Locate every leukocyte (white blood cell).
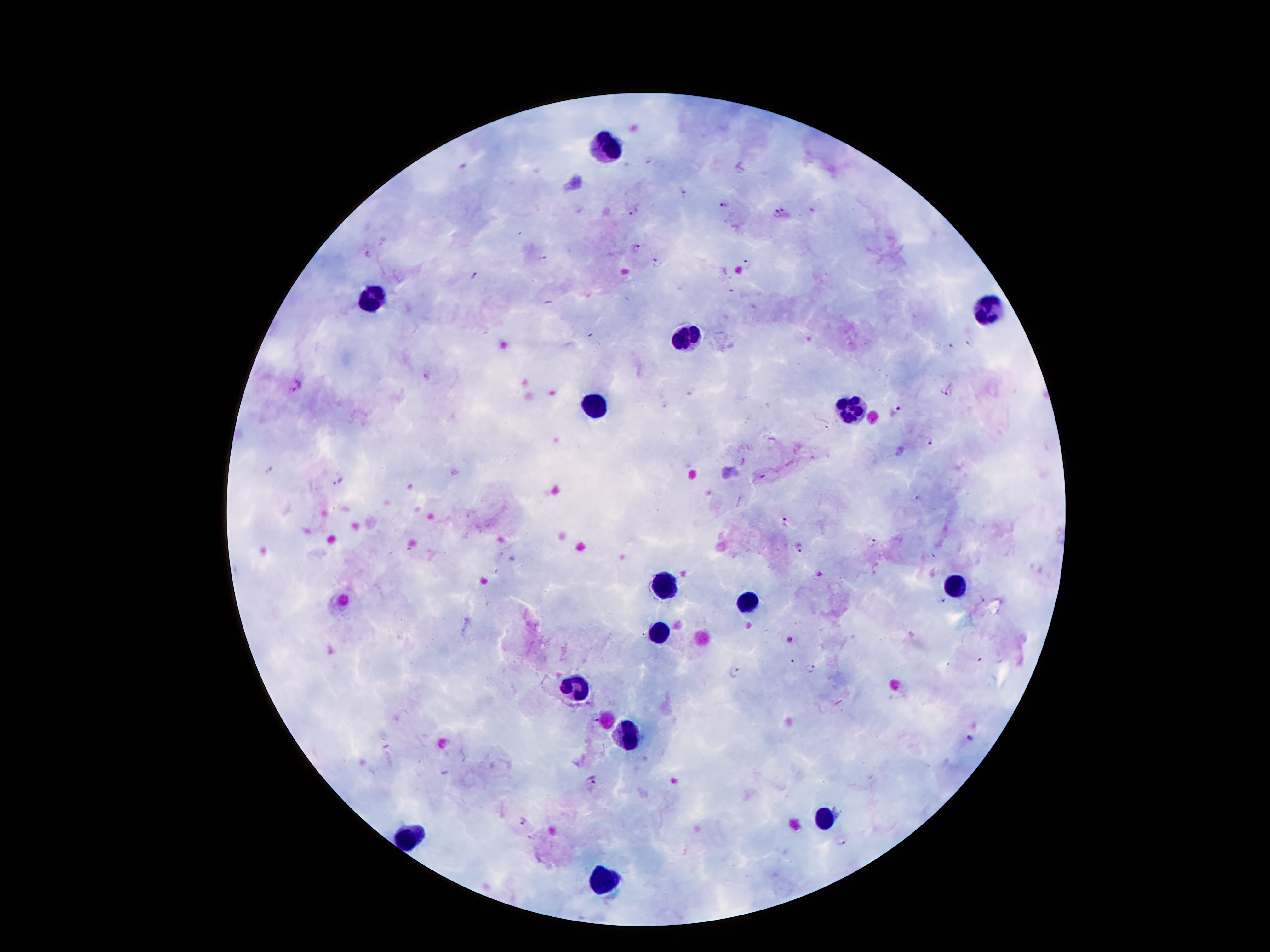
Approximate object centers, in pixels from the top-left corner.
Leukocytes: (x=609, y=144), (x=370, y=301), (x=988, y=307), (x=687, y=338), (x=853, y=406), (x=596, y=407), (x=669, y=582), (x=956, y=585), (x=745, y=604), (x=657, y=632), (x=579, y=688), (x=626, y=738), (x=824, y=815), (x=415, y=836), (x=607, y=882).

image_size: 1270×952 pixels
stain: Giemsa
patient_malaria_status: positive for Plasmodium falciparum
field_of_view: single
magnification: 100x
malaria_parasite_locations: 'approximate object centers, in pixels from the top-left corner: (x=648, y=159), (x=684, y=193), (x=723, y=201), (x=632, y=210), (x=780, y=213), (x=638, y=248), (x=366, y=254), (x=541, y=258), (x=656, y=261), (x=748, y=264), (x=475, y=278), (x=969, y=342), (x=951, y=345), (x=428, y=377), (x=301, y=383), (x=289, y=391), (x=949, y=391), (x=900, y=409), (x=826, y=424), (x=930, y=442), (x=268, y=469), (x=338, y=480), (x=915, y=499), (x=786, y=522), (x=870, y=543), (x=800, y=547), (x=941, y=600), (x=792, y=661), (x=810, y=669), (x=734, y=673), (x=970, y=740), (x=592, y=782), (x=521, y=822), (x=841, y=842)'
preparation: thick blood film
capture: smartphone camera through the microscope eyepiece